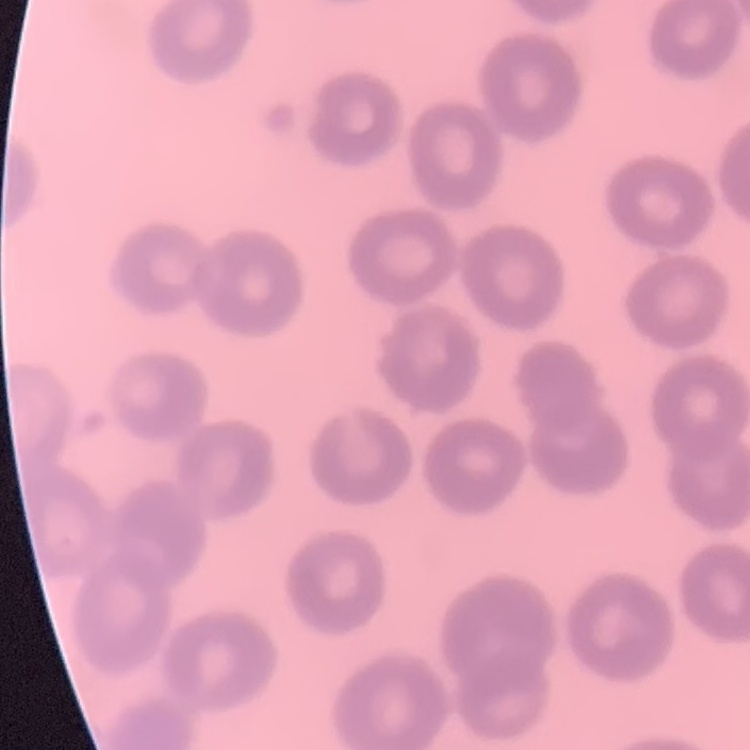

red blood cell morphology = no rouleaux formation
stain = Field's or Giemsa
image type = one tile cut from a larger photomicrograph
preparation = thin peripheral smear